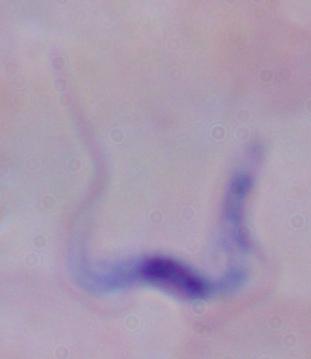
Summary:
  - Magnification: 1000x
  - Modality: micrograph
  - Identification: trypanosome